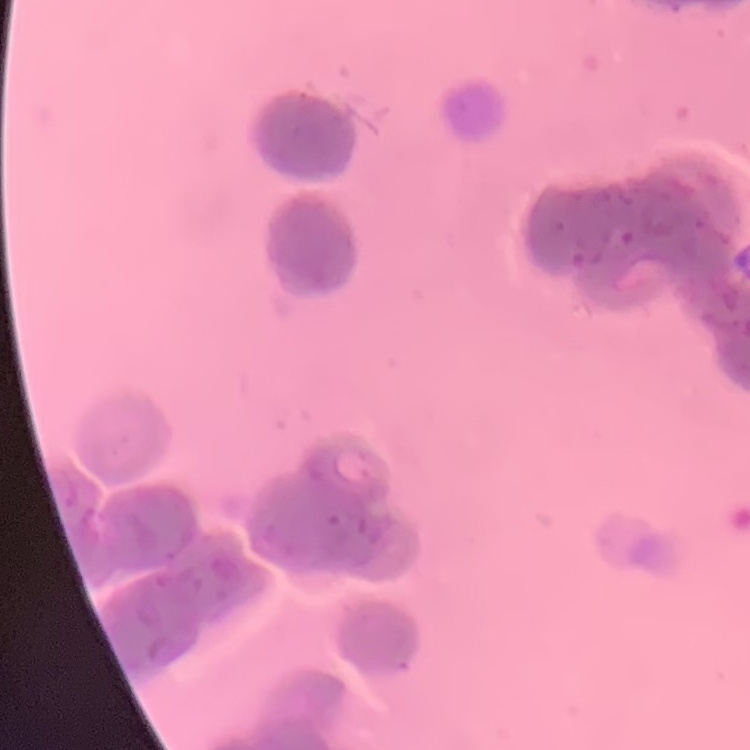

The erythrocytes exhibit rouleaux formation. Thin peripheral smear. Square crop of a larger photomicrograph. Stained with either Field's or Giemsa.